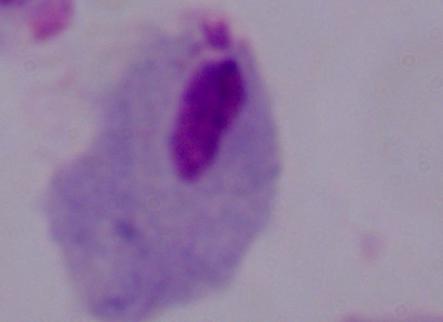
Summary:
  - Magnification: 1000x
  - Identification: trichomonad
  - Modality: micrograph